Look for Plasmodium parasites.
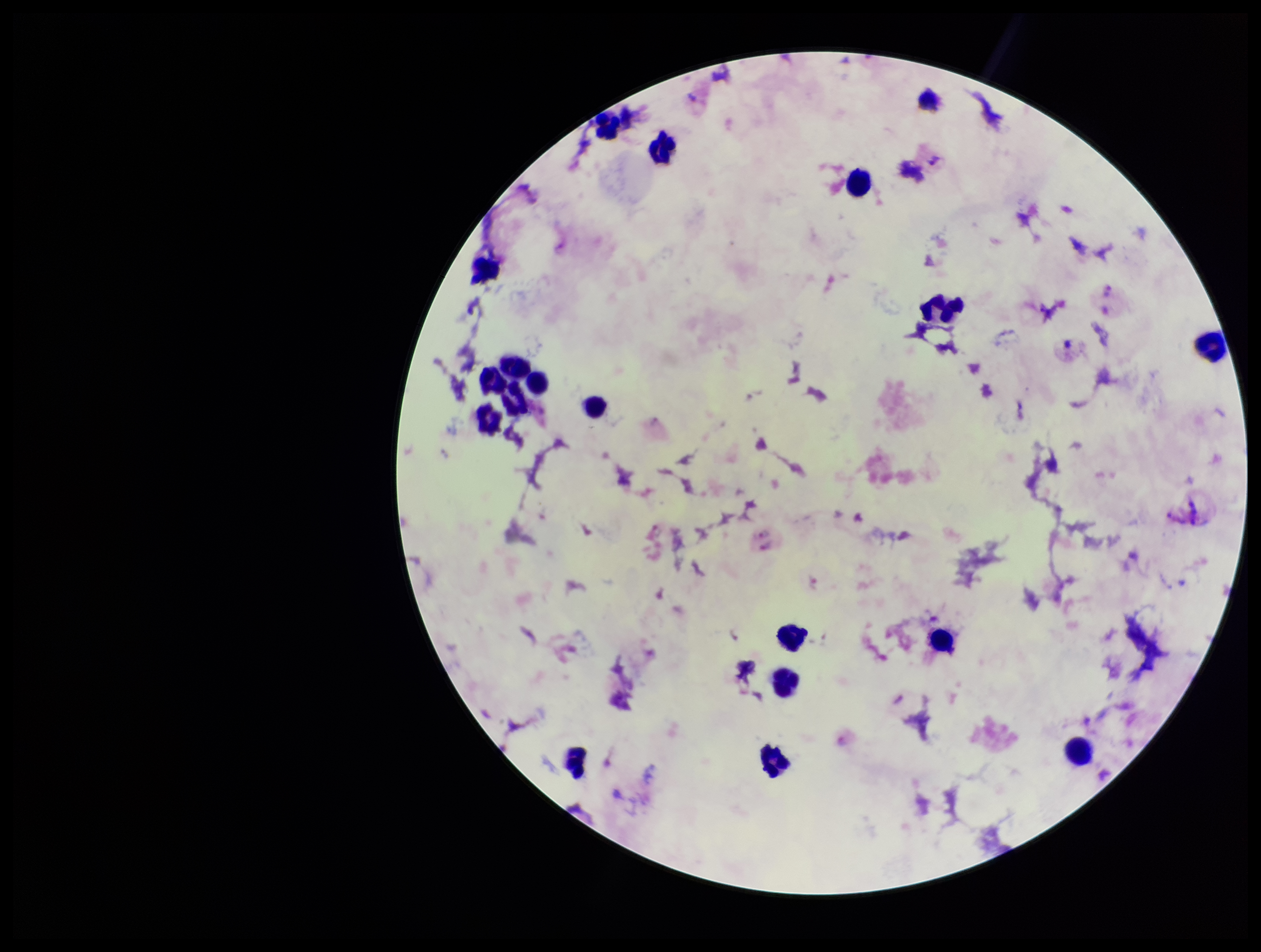
None detected.

Summary:
  - Species reported for this patient: Plasmodium vivax
  - Parasite count: 0
  - Patient malaria status: infected
  - Image size: 1261×952 pixels
  - Field of view: single
  - Capture: smartphone photograph through the microscope eyepiece
  - Preparation: thick
  - Stain: Giemsa
  - Leukocyte count: 19